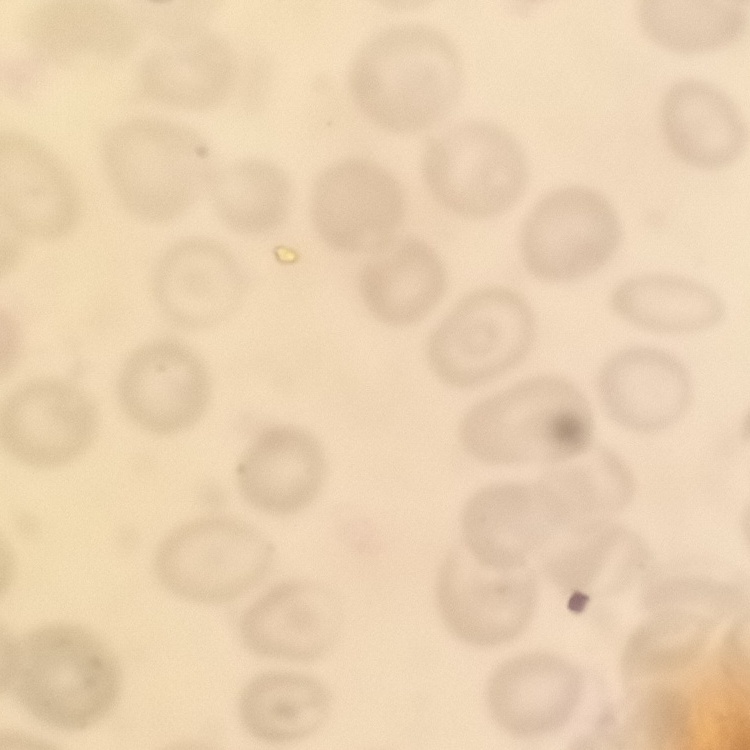

Summary:
  - Erythrocyte morphology: no rouleaux formation
  - Stain: Field's or Giemsa
  - Image type: square crop of a larger photomicrograph
  - Preparation: thin peripheral smear